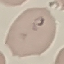

malaria status = parasitized
stain = Giemsa
image type = automatically extracted cell patch, resized to 64 × 64 pixels
preparation = thin blood film
capture = smartphone camera at the microscope eyepiece